Identify the parasite.
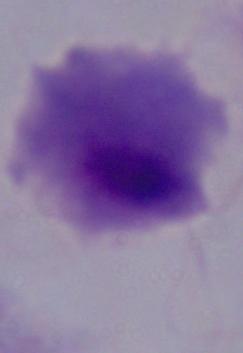
This is a trichomonad.

Summary:
  - Magnification: 1000x
  - Modality: micrograph